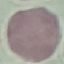

malaria status = uninfected
stain = Giemsa
preparation = thin blood smear
image type = cell patch, automatically extracted from a larger field of view and resized to 64 × 64 pixels
capture = smartphone camera at the microscope eyepiece